State which cell type is depicted.
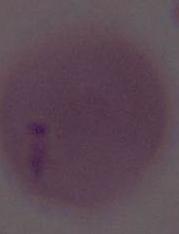
This is an erythrocyte.

Photomicrograph. 1000x magnification.